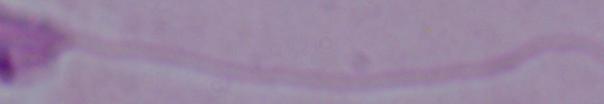

Summary:
  - Magnification: 1000x
  - Identification: Leishmania
  - Modality: photomicrograph